Report the malaria status of this cell.
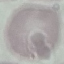

Uninfected.

Summary:
  - Capture: smartphone through the microscope eyepiece
  - Image type: cell patch, automatically extracted from a larger field of view and resized to 64 × 64 pixels
  - Preparation: thin smear
  - Stain: Giemsa